Give the position of every Plasmodium parasite visible.
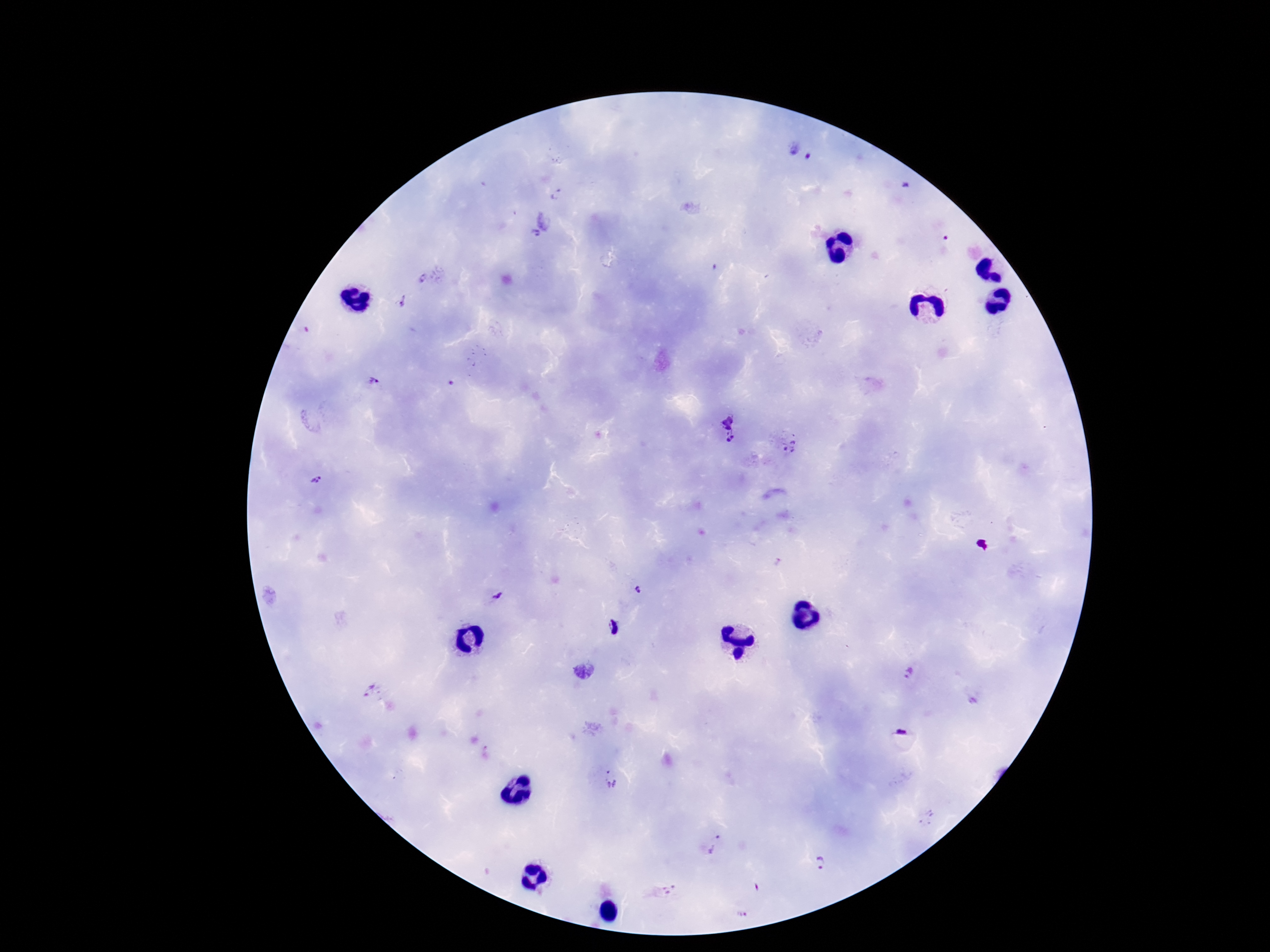
Approximate object centers, in pixels from the top-left corner.
Plasmodium parasites: (x=801, y=152), (x=556, y=194), (x=544, y=220), (x=536, y=234), (x=422, y=280), (x=403, y=301), (x=373, y=382), (x=728, y=429), (x=790, y=446), (x=317, y=481), (x=637, y=590), (x=496, y=594), (x=615, y=627), (x=908, y=673), (x=370, y=692), (x=972, y=700), (x=903, y=731), (x=612, y=778), (x=715, y=844), (x=820, y=863), (x=757, y=887), (x=670, y=889), (x=742, y=913).

Summary:
  - Field of view: single
  - Capture: smartphone camera through the microscope eyepiece
  - Patient malaria status: infected
  - Stain: Giemsa
  - Magnification: 100x
  - Preparation: thick blood film
  - Image size: 1270×952 pixels